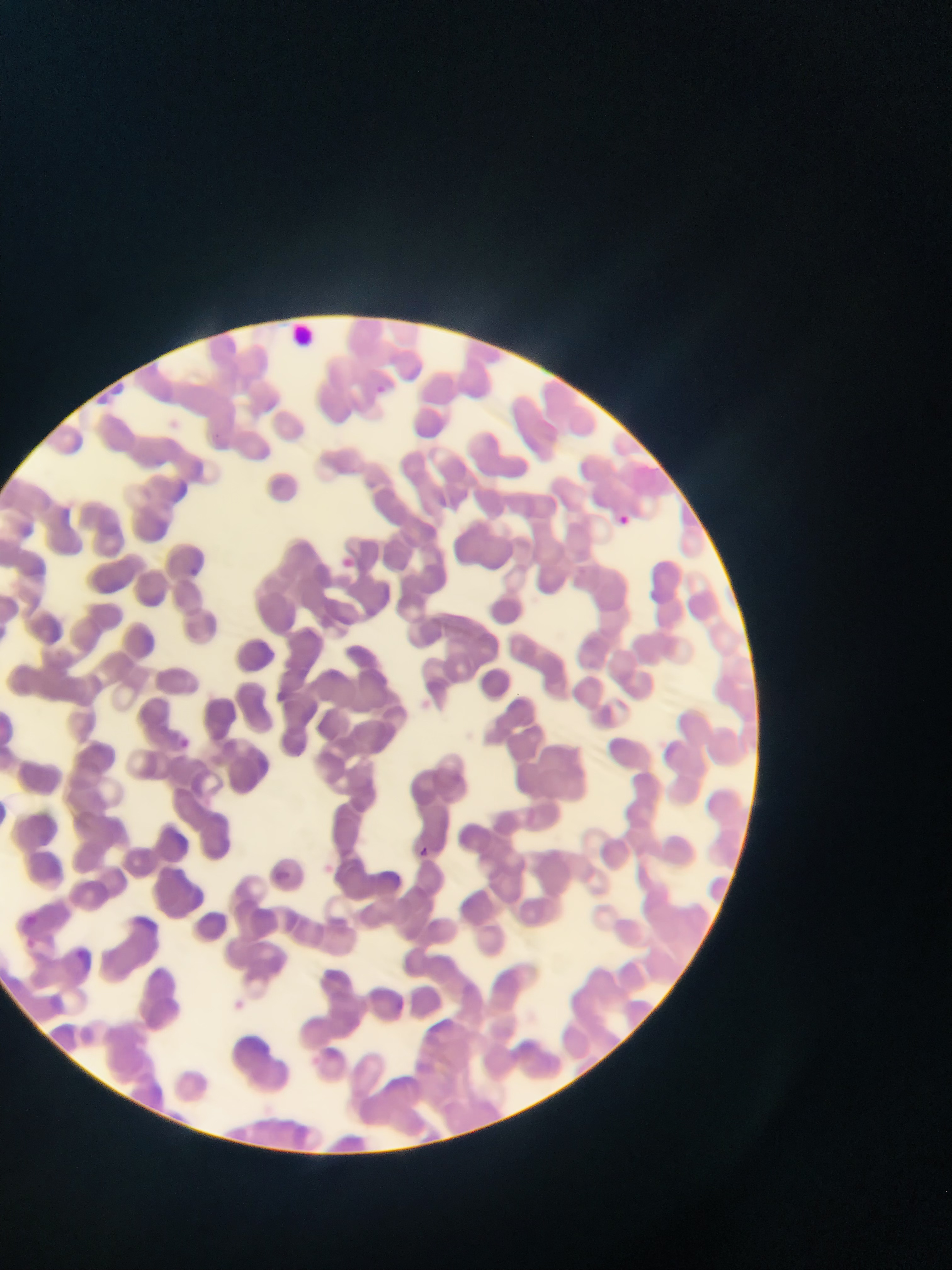
Approximate bounding boxes as left top right bottom in pixels.
Summary:
  - Leukocyte locations: 289 321 313 346
  - Malaria parasite locations: 376 383 385 395; 620 513 639 532; 418 842 433 857
  - Capture: mobile-phone photograph through a microscope
  - Field of view: single
  - Image size: 952×1270 pixels
  - Country: Ghana
  - Preparation: thin blood smear